Classify this cell by malaria status.
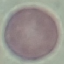

It is uninfected.

Summary:
  - Capture: smartphone camera at the microscope eyepiece
  - Stain: Giemsa
  - Preparation: thin blood film
  - Image type: automatically extracted cell patch, resized to 64 × 64 pixels